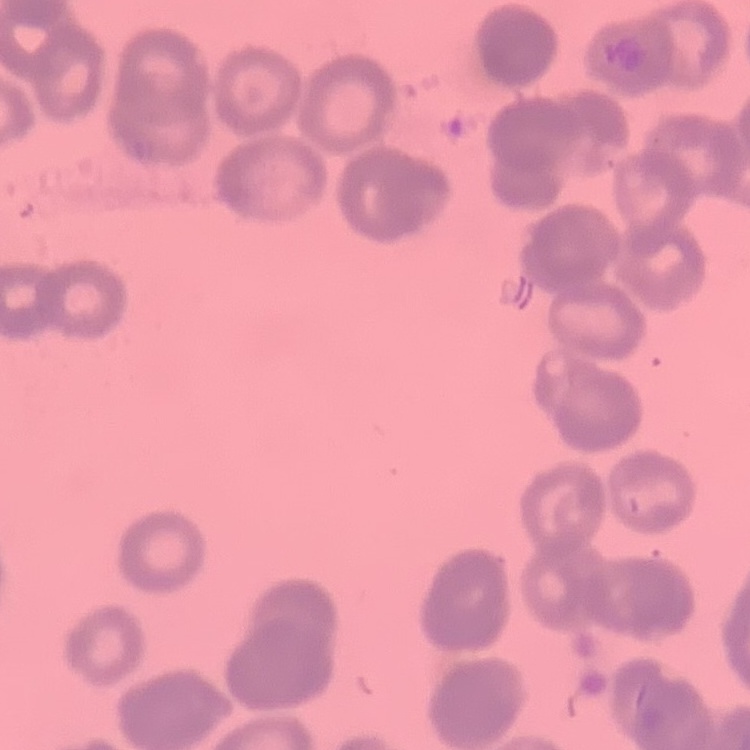
The erythrocytes exhibit rouleaux formation. Stained with either Field's or Giemsa. Thin blood film. One tile cut from a larger photomicrograph.